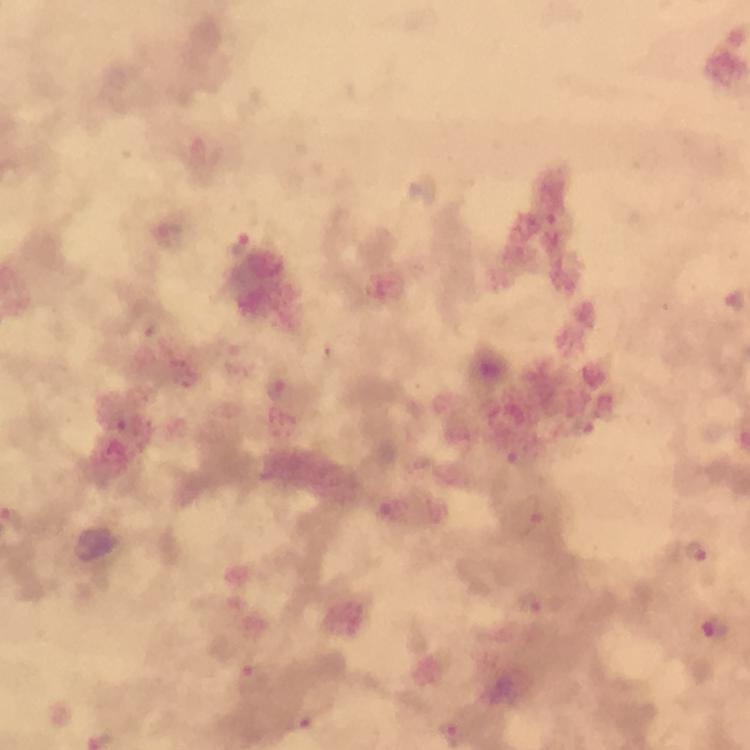

Approximate centers as {x, y} in pixels. Malaria parasite locations: {239, 242}, {735, 299}, {583, 428}, {521, 457}, {527, 516}, {695, 552}, {530, 603}, {716, 626}, {250, 677}, {300, 719}, {449, 733}. From a diagnostic examination for malaria. At 100x magnification. Giemsa-stained preparation. Thick blood smear. Immersion oil applied. Image is 750×750 pixels. A crop from one field of view. Photographed through the microscope with a smartphone camera.